State the preparation type.
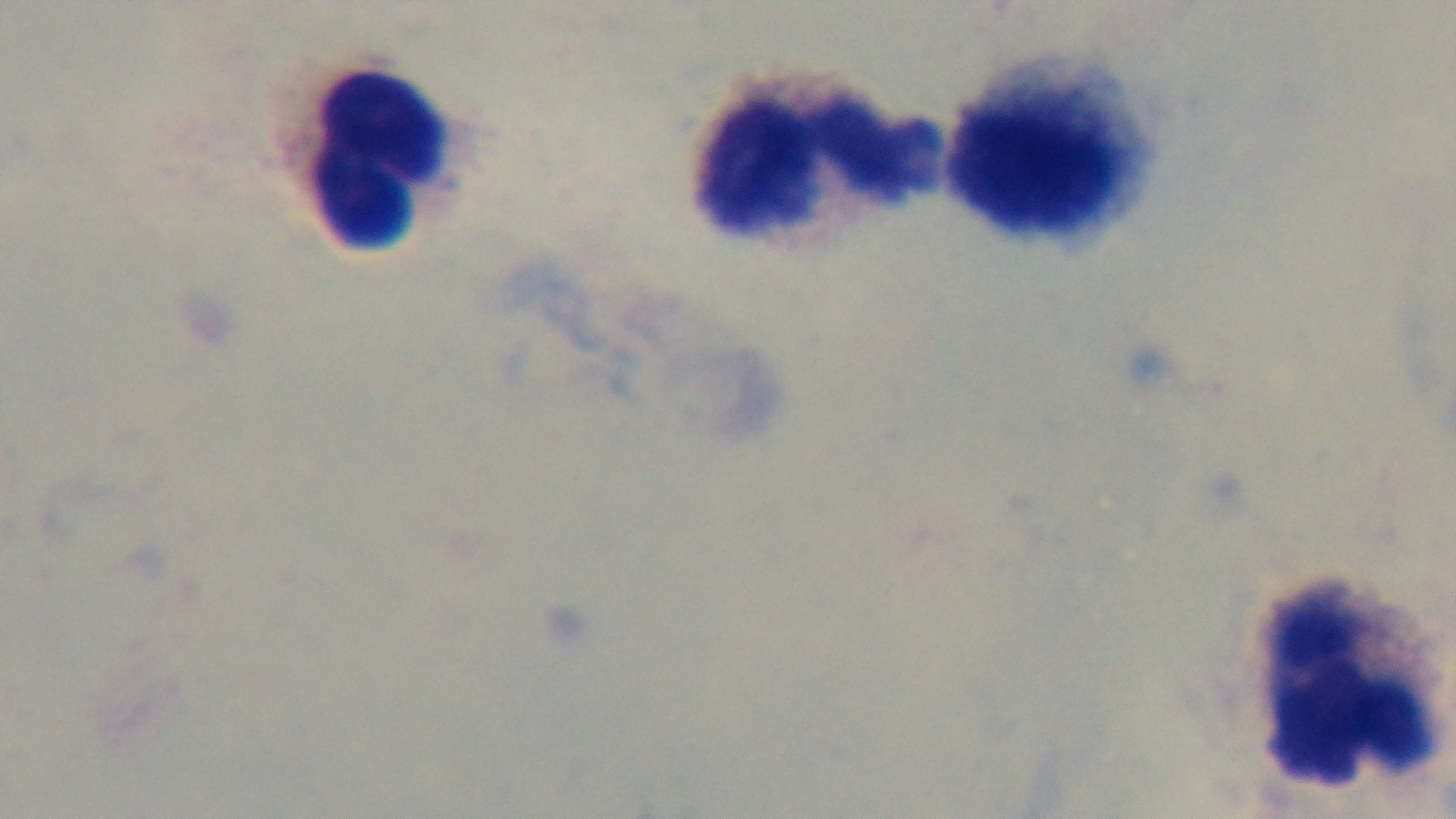

It is a thick blood film.

field of view = single
modality = light microscopy
malaria status = negative
capture = mounted 4K digital camera
objective = 100x oil immersion
stain = Giemsa